Classify this cell by malaria status.
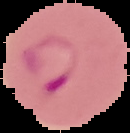

Parasitized.

Cell region segmented out of the field of view; the surrounding area is masked to black. Image is 130×133 pixels. From a thin blood film.